Outline each blood parasite and name the species.
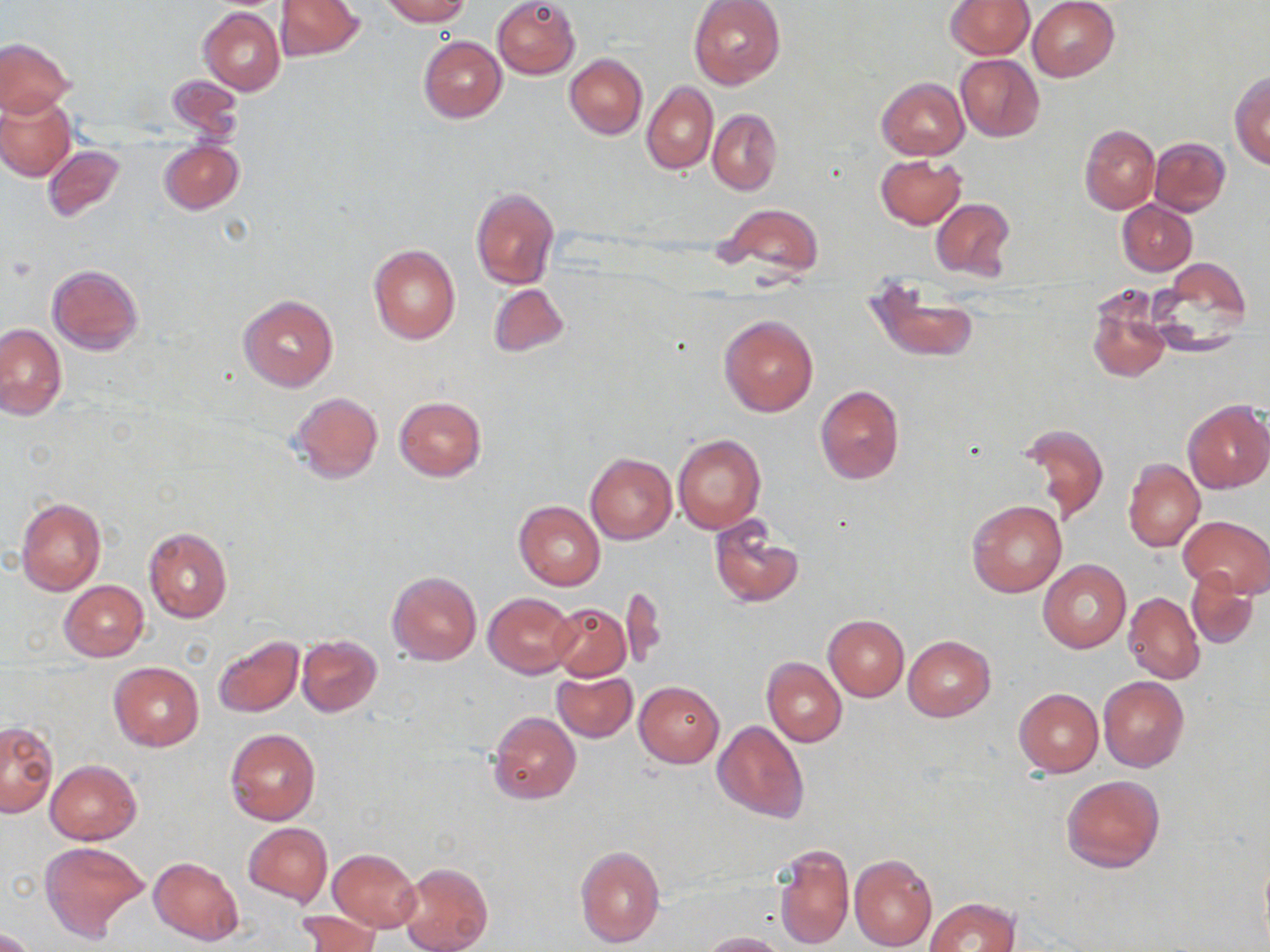

No blood parasites seen.

Approximate bounding boxes as (x1, y1, x2, y2) in pixels. Uninfected red blood cell locations: (277, 0, 365, 60), (380, 0, 469, 25), (492, 0, 580, 79), (688, 0, 786, 89), (1028, 0, 1120, 82), (945, 1, 1033, 59), (199, 7, 284, 95), (418, 35, 506, 123), (0, 38, 74, 117), (565, 54, 646, 139), (956, 55, 1044, 141), (1229, 70, 1270, 168), (166, 76, 242, 142), (877, 77, 969, 160), (642, 81, 718, 175), (0, 93, 75, 181), (645, 98, 782, 184), (708, 109, 781, 194), (1080, 124, 1161, 214), (1150, 137, 1230, 215), (159, 142, 243, 214), (43, 145, 125, 223), (875, 155, 965, 229), (470, 186, 558, 290), (930, 198, 1015, 282), (1117, 200, 1197, 275), (716, 203, 825, 279), (369, 243, 461, 344), (1148, 259, 1252, 355), (46, 265, 143, 356), (866, 277, 978, 364), (487, 283, 568, 357), (1087, 293, 1171, 384), (239, 296, 336, 391), (719, 314, 818, 417), (0, 323, 66, 419), (815, 385, 905, 485), (290, 391, 383, 485), (394, 397, 487, 481), (1183, 400, 1270, 494), (1016, 422, 1109, 525), (673, 434, 765, 534), (585, 453, 676, 544), (1123, 458, 1205, 552), (15, 496, 106, 596), (514, 500, 605, 590), (966, 500, 1066, 598), (1180, 515, 1270, 596), (709, 518, 800, 608), (143, 526, 232, 623), (1039, 560, 1130, 654), (1184, 566, 1259, 650), (386, 570, 481, 666), (59, 581, 149, 660), (620, 585, 667, 670), (484, 592, 578, 677), (1124, 592, 1204, 685), (549, 603, 631, 681), (823, 615, 909, 700), (213, 635, 303, 718), (296, 635, 381, 716), (903, 635, 995, 722), (762, 657, 847, 749), (108, 662, 204, 752), (552, 670, 637, 742), (1099, 678, 1189, 772), (634, 682, 723, 767), (1014, 688, 1103, 777), (488, 711, 582, 805), (713, 719, 808, 823), (1, 724, 57, 818), (225, 728, 320, 825), (45, 760, 141, 845), (1061, 774, 1165, 873), (243, 822, 333, 907), (39, 841, 149, 944), (772, 842, 854, 950), (576, 846, 665, 947), (328, 849, 422, 931), (1258, 850, 1269, 950), (849, 853, 937, 951), (149, 857, 243, 945), (398, 861, 492, 952), (924, 898, 1019, 952), (297, 910, 381, 952), (0, 927, 38, 952), (700, 931, 785, 951). Slide-level diagnosis: no evidence of blood parasites. Single field of view. Image is 1270×952 pixels. Thin blood film. Captured at 1000x magnification. Optical microscopy. May-Grünwald-Giemsa-stained preparation.